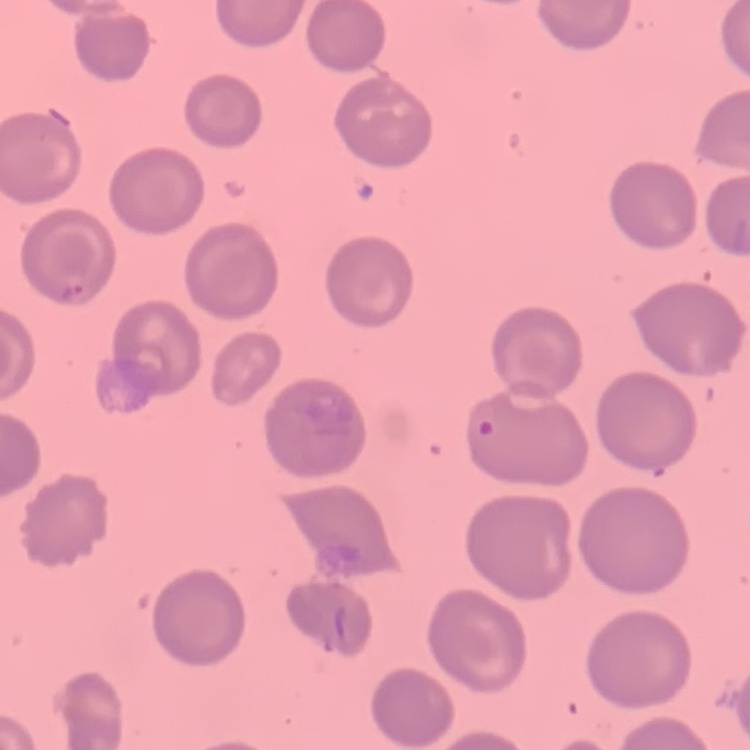
erythrocyte morphology = no rouleaux formation
preparation = thin blood smear
image type = one tile cut from a larger photomicrograph
stain = Field's or Giemsa